Outline each blood parasite and name the species.
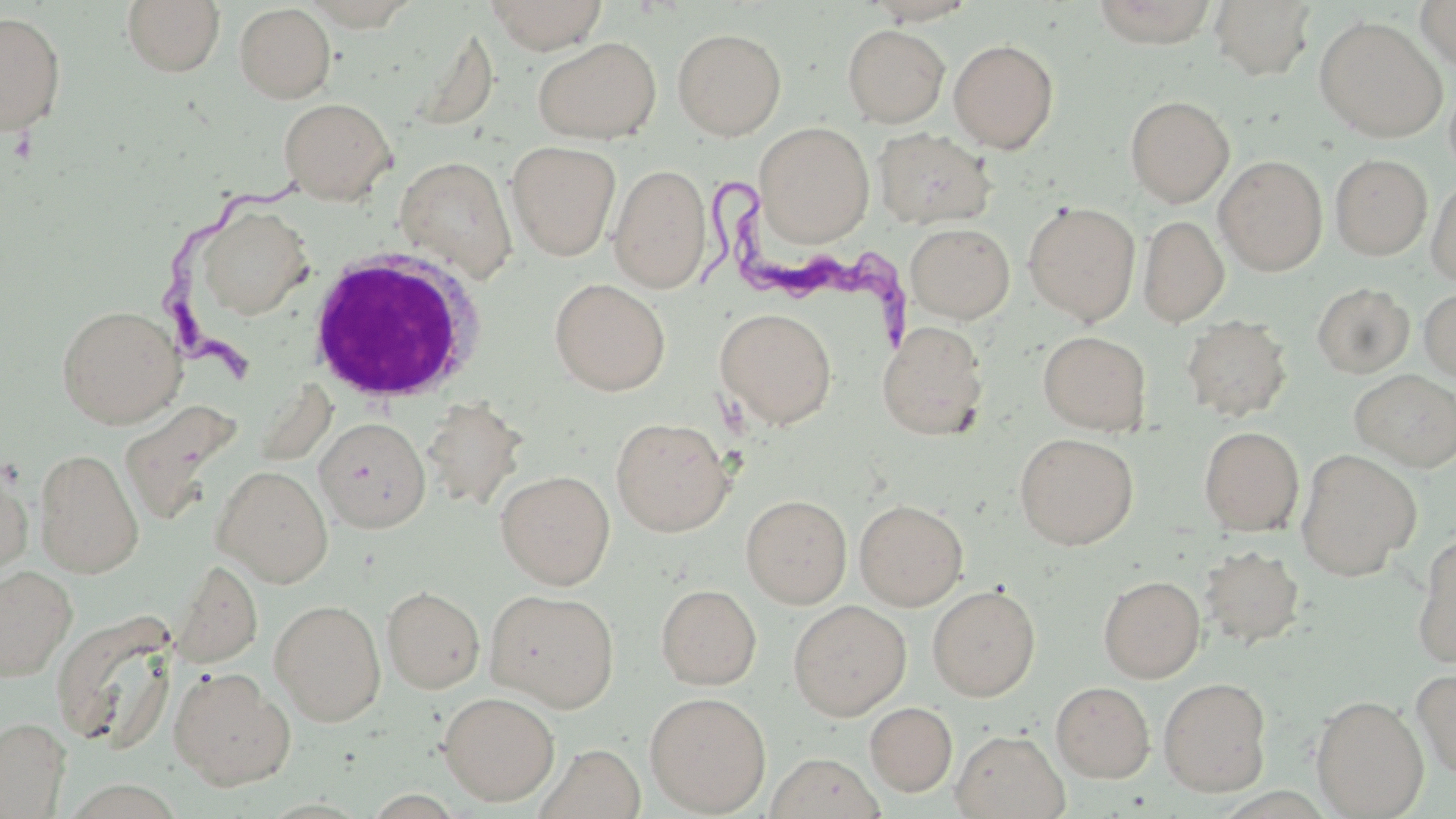
Approximate bounding boxes as [x1, y1, x2, y2] in pixels.
Trypanosoma brucei: [161, 169, 306, 377], [705, 179, 928, 348].
No Plasmodium falciparum, Plasmodium ovale, Plasmodium malariae, Plasmodium vivax, or Babesia divergens observed.

Uninfected red blood cell locations: [122, 0, 226, 77], [485, 0, 608, 53], [1208, 0, 1317, 81], [1089, 1, 1220, 47], [1415, 1, 1456, 71], [234, 4, 336, 103], [0, 10, 66, 135], [1314, 16, 1447, 142], [407, 24, 499, 133], [842, 24, 950, 127], [672, 27, 787, 140], [532, 37, 662, 144], [949, 39, 1059, 152], [1125, 95, 1234, 206], [279, 97, 396, 204], [754, 122, 874, 245], [873, 127, 997, 229], [507, 140, 621, 261], [1330, 154, 1432, 260], [395, 155, 517, 283], [1215, 156, 1327, 275], [610, 164, 711, 291], [1426, 174, 1456, 287], [1023, 201, 1140, 324], [196, 204, 313, 320], [1138, 215, 1229, 327], [906, 222, 1015, 322], [550, 278, 670, 395], [1312, 282, 1415, 378], [1418, 287, 1456, 382], [57, 304, 185, 428], [715, 307, 838, 429], [1179, 314, 1293, 422], [877, 321, 989, 440], [1038, 330, 1152, 435], [1350, 369, 1456, 472], [422, 397, 526, 512], [315, 417, 431, 532], [610, 417, 736, 536], [1199, 426, 1304, 536], [1015, 432, 1138, 549], [34, 447, 144, 577], [1295, 449, 1421, 581], [0, 464, 32, 581], [212, 464, 333, 587], [496, 470, 615, 589], [741, 494, 852, 608], [855, 499, 968, 611], [1412, 532, 1456, 668], [1199, 544, 1305, 649], [169, 559, 263, 669], [0, 564, 77, 681], [1098, 575, 1205, 683], [656, 584, 762, 689], [927, 584, 1041, 701], [382, 585, 485, 694], [485, 589, 620, 711], [270, 599, 386, 726], [788, 600, 911, 720], [50, 611, 180, 750], [168, 667, 295, 788], [1412, 667, 1456, 780], [1159, 677, 1272, 796], [1051, 681, 1155, 782], [438, 691, 560, 805], [644, 691, 771, 815], [1311, 695, 1429, 818], [865, 701, 957, 797], [0, 717, 71, 817], [952, 729, 1069, 819], [538, 743, 645, 819], [765, 752, 887, 819]. White blood cell locations: [302, 248, 488, 405]. Slide-level diagnosis: Trypanosoma brucei. Image is 1456×819 pixels. May-Grünwald-Giemsa-stained preparation. Captured at 1000x magnification. Single field of view. Thin blood smear. Light microscopy.